Give the position of every Plasmodium parasite visible.
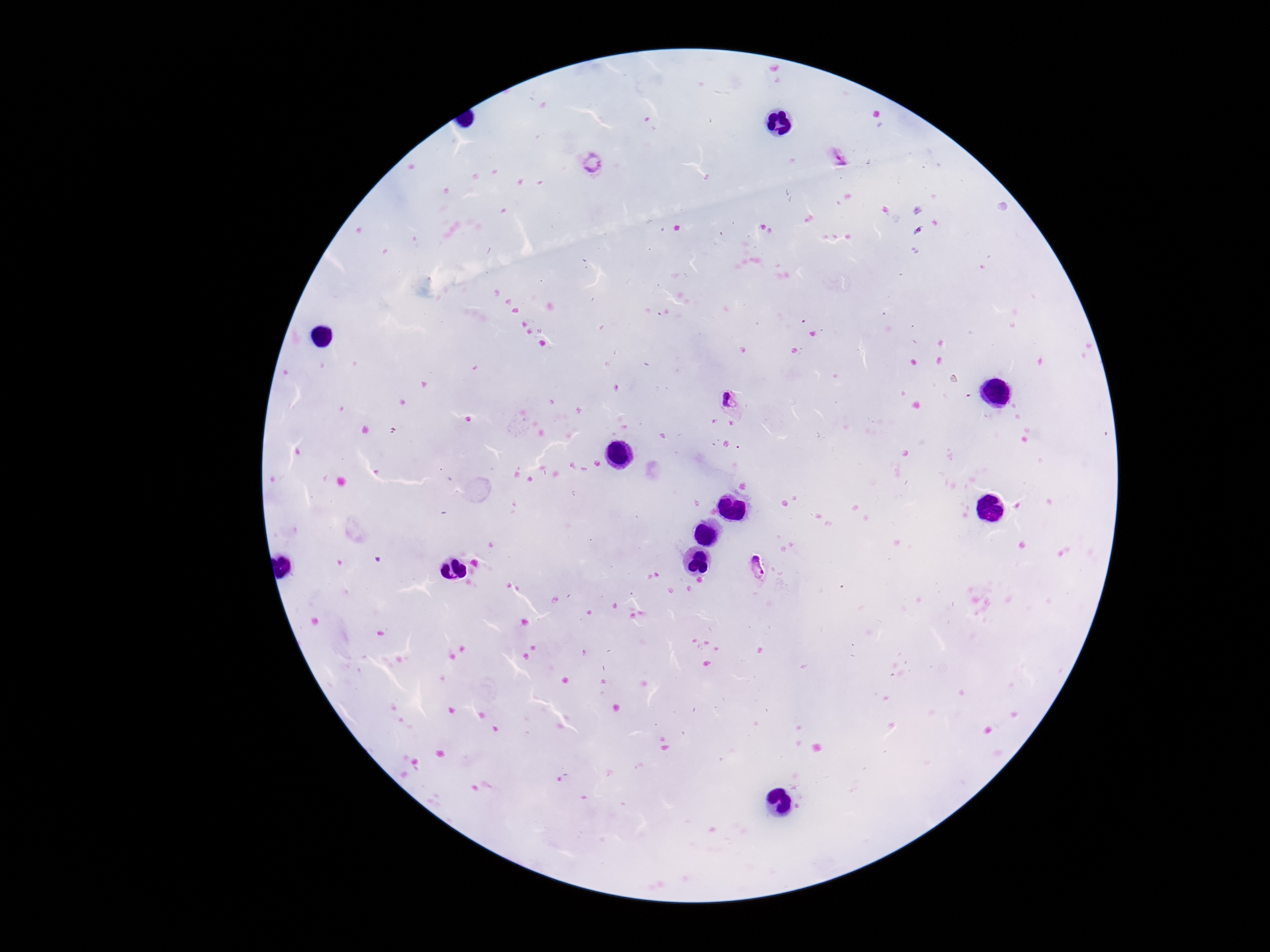
Approximate object centers, in pixels from the top-left corner.
Plasmodium parasites: (x=839, y=158), (x=591, y=166), (x=732, y=405), (x=760, y=571).

Smartphone photograph taken through the microscope eyepiece. Single field of view. 100x magnification. Giemsa stain. Patient malaria status: positive. Image is 1270×952 pixels. Thick peripheral-blood smear.